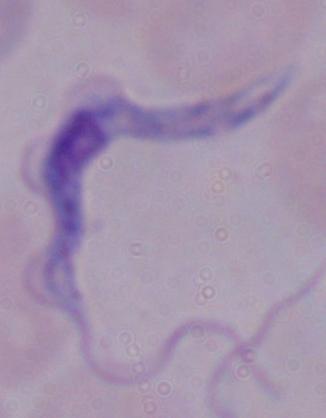
A trypanosome is seen. 1000x magnification. Micrograph.